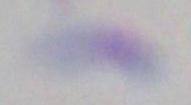
modality = photomicrograph
identification = Toxoplasma gondii
magnification = 1000x